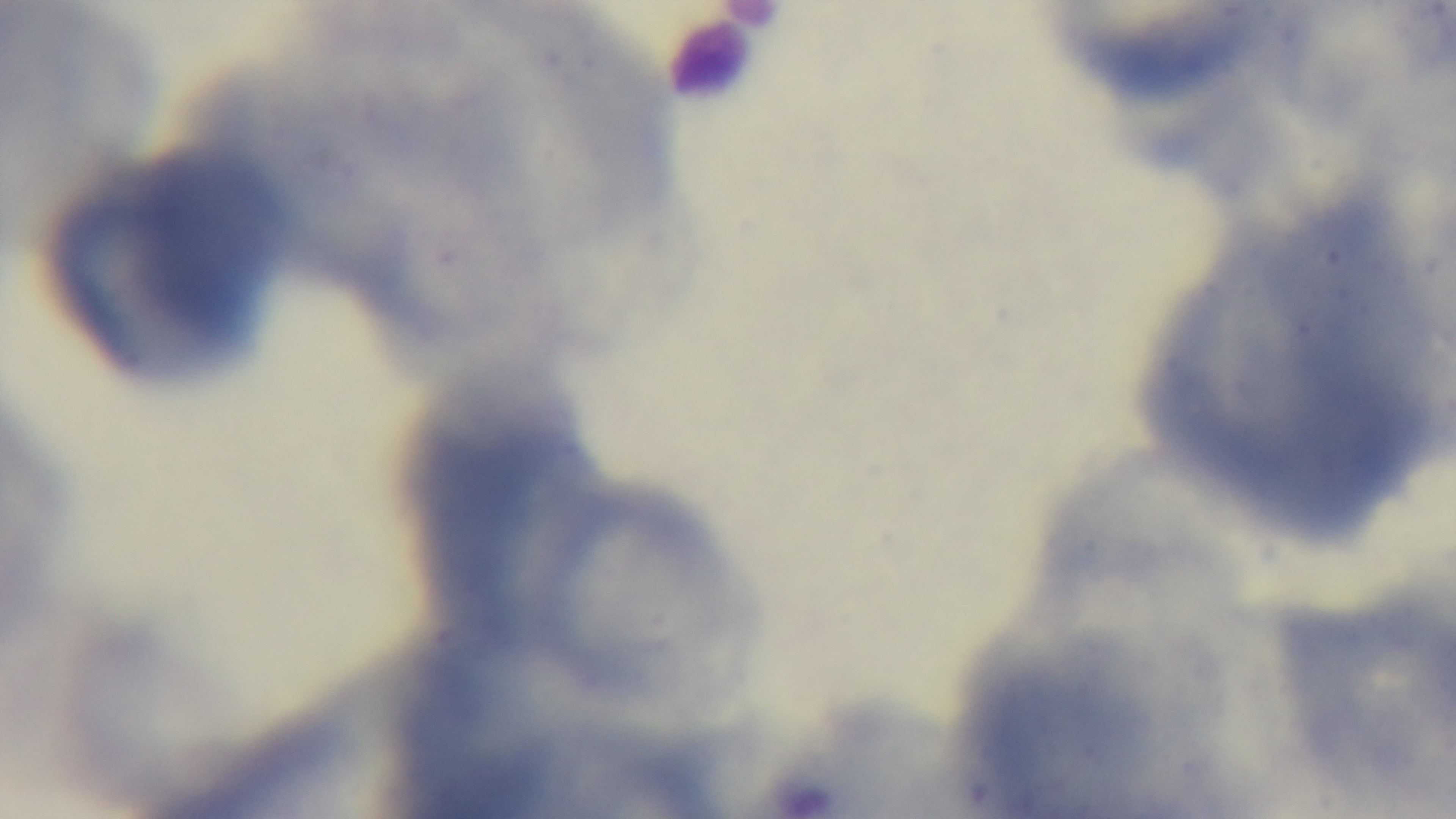

capture: mounted 4K digital camera
field_of_view: single
stain: Giemsa
objective: 100x oil immersion
malaria_status: uninfected
modality: light microscopy
preparation: thin blood film